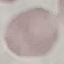
Summary:
  - Malaria status: uninfected
  - Image type: automatically extracted cell patch, resized to 64 × 64 pixels
  - Stain: Giemsa
  - Capture: smartphone through the microscope eyepiece
  - Preparation: thin blood smear